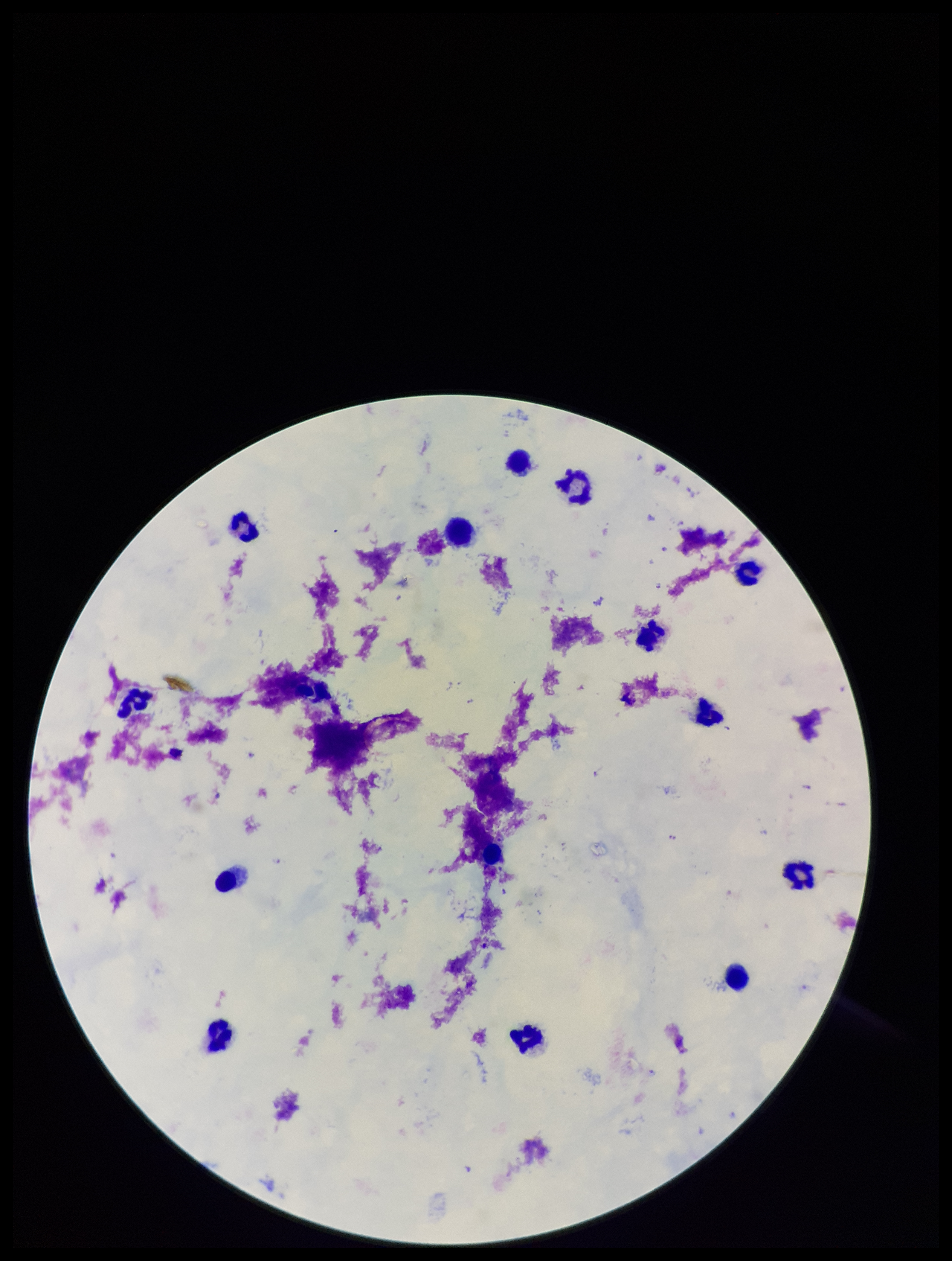
preparation = thick blood smear
patient malaria status = positive
field of view = one from this slide
stain = Giemsa
parasite count = 7
capture = smartphone photograph through the microscope eyepiece
Plasmodium parasites = identified
leukocyte count = 13
image size = 952×1261 pixels
species reported for this patient = Plasmodium falciparum